Outline each blood parasite and name the species.
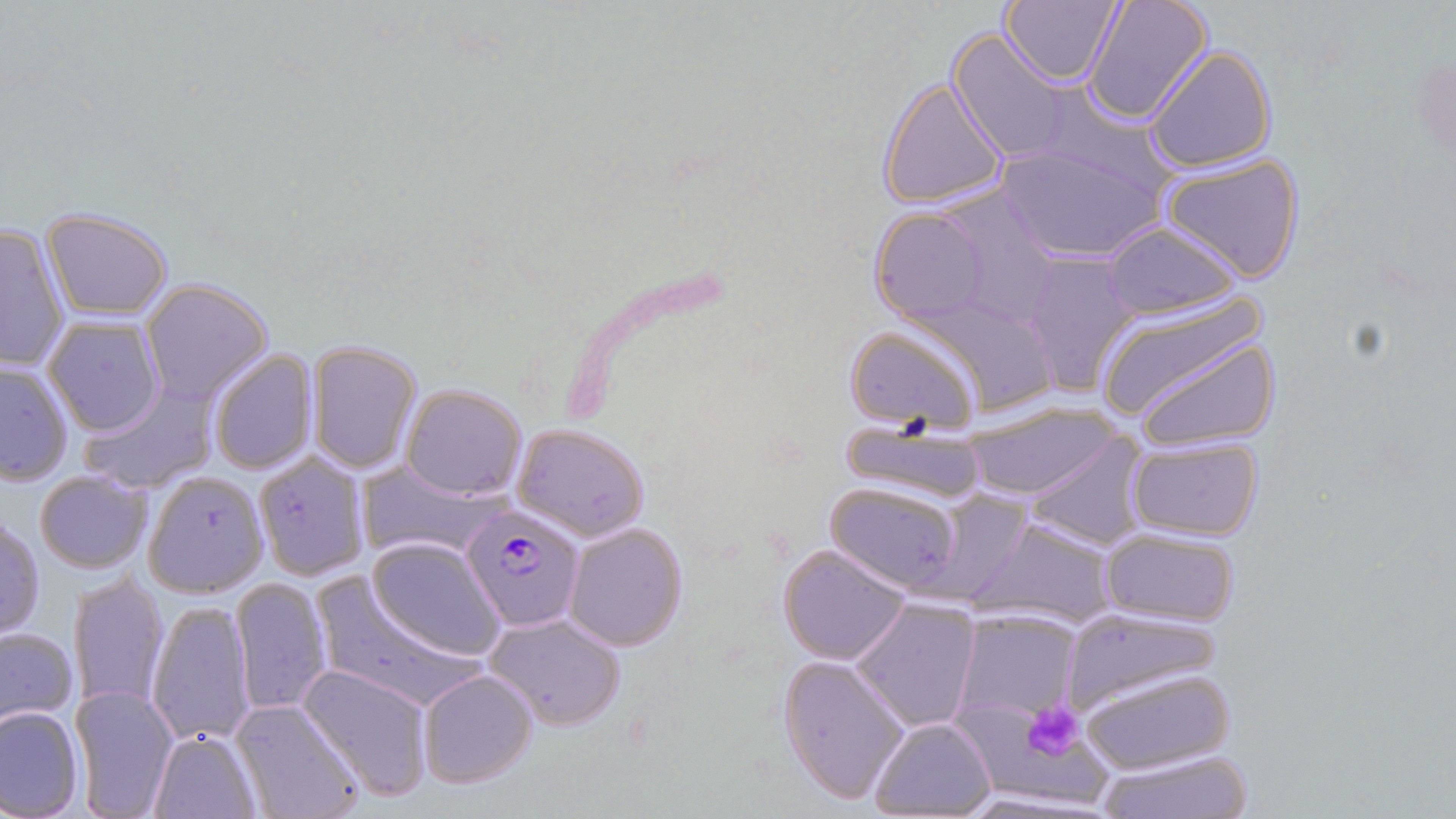
Approximate bounding boxes as [x1, y1, x2, y2] in pixels.
Plasmodium falciparum-infected red blood cells: [460, 504, 586, 630].
No Plasmodium ovale, Plasmodium malariae, Plasmodium vivax, Babesia divergens, or Trypanosoma brucei observed.

Summary:
  - Uninfected red blood cell locations: [1001, 0, 1124, 88], [1083, 0, 1214, 127], [946, 29, 1076, 166], [1142, 44, 1276, 173], [1403, 57, 1456, 162], [878, 76, 1010, 210], [994, 142, 1165, 262], [1159, 151, 1307, 283], [870, 206, 992, 326], [42, 209, 174, 320], [1099, 218, 1246, 320], [0, 223, 72, 371], [1020, 256, 1142, 395], [141, 278, 273, 407], [1089, 295, 1271, 426], [43, 314, 165, 436], [842, 324, 980, 430], [1133, 334, 1283, 453], [305, 340, 423, 475], [207, 348, 317, 475], [0, 361, 74, 485], [79, 382, 218, 495], [400, 382, 527, 500], [959, 403, 1118, 501], [840, 420, 994, 507], [512, 422, 650, 541], [1021, 435, 1147, 550], [1125, 436, 1264, 542], [260, 453, 377, 579], [361, 461, 490, 561], [33, 469, 152, 573], [142, 470, 267, 597], [825, 480, 967, 594], [0, 516, 44, 640], [969, 518, 1119, 628], [563, 522, 689, 652], [1097, 528, 1243, 628], [367, 538, 505, 659], [778, 545, 911, 664], [70, 568, 169, 715], [230, 577, 333, 717], [306, 577, 485, 711], [850, 597, 981, 733], [148, 600, 255, 746], [1058, 608, 1223, 717], [952, 609, 1083, 723], [483, 612, 628, 732], [0, 627, 77, 730], [778, 653, 911, 804], [299, 663, 434, 800], [1074, 665, 1234, 776], [417, 670, 538, 789], [72, 685, 178, 817], [232, 700, 363, 819], [0, 703, 85, 817], [959, 703, 1111, 810], [868, 717, 996, 817], [148, 729, 260, 817], [1090, 746, 1255, 818], [951, 788, 1116, 818]
  - Platelet locations: [1021, 701, 1086, 761]
  - Slide-level diagnosis: Plasmodium falciparum
  - Field of view: one of a larger specimen
  - Image size: 1456×819 pixels
  - Modality: optical microscopy
  - Stain: May-Grünwald-Giemsa
  - Magnification: 1000x
  - Preparation: thin blood film